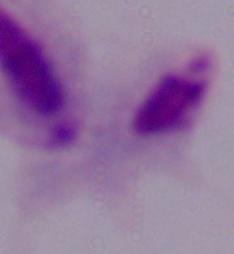

magnification = 1000x
identification = trichomonad
modality = photomicrograph